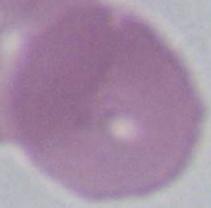

Summary:
  - Identification: red blood cell
  - Magnification: 1000x
  - Modality: photomicrograph